Assess this cell for malaria.
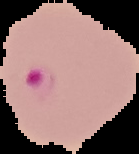
Parasitized.

image type = cell region segmented out of the field of view; surrounding area masked to black
image size = 139×154 pixels
preparation = thin blood smear